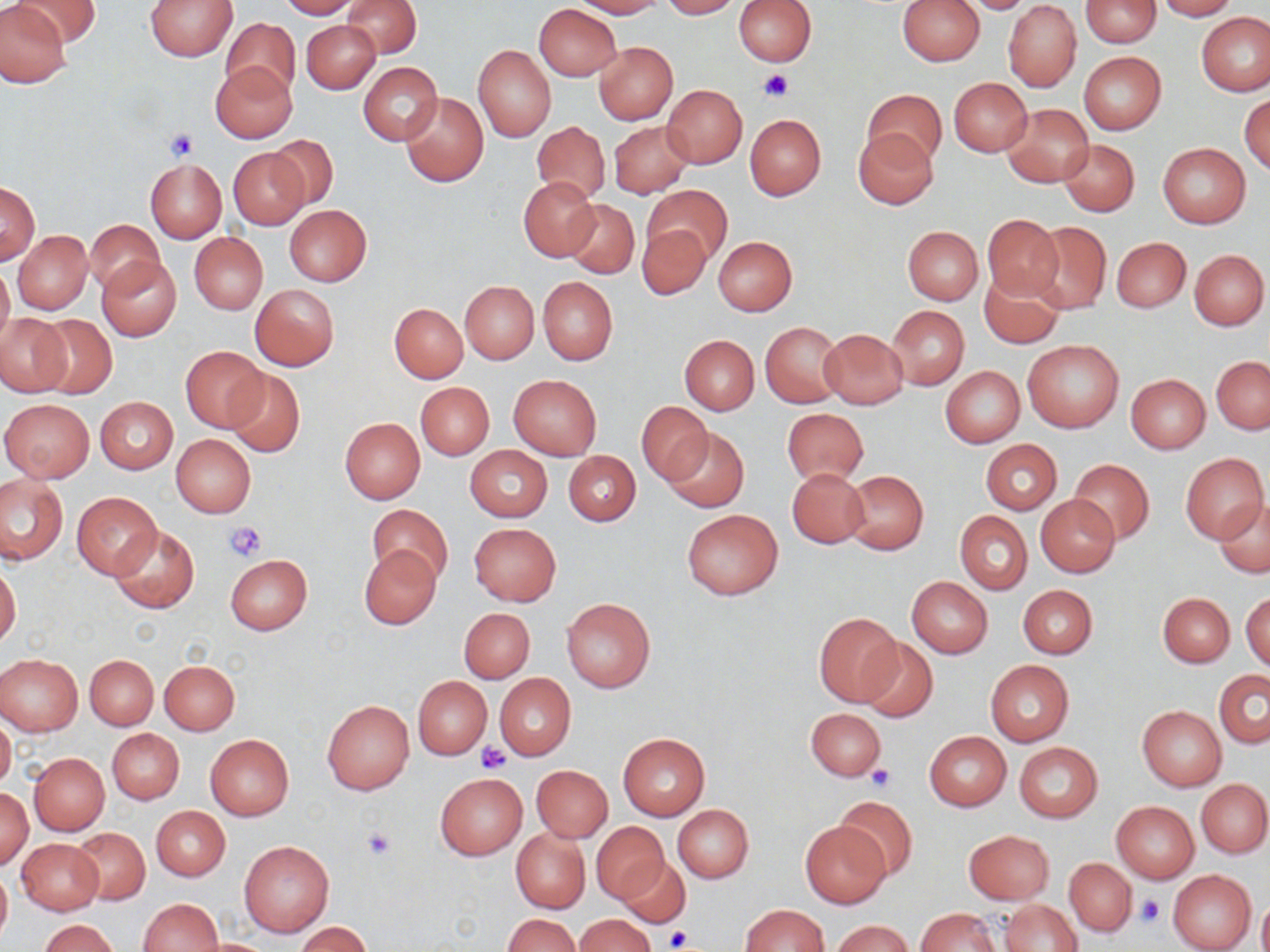

slide-level diagnosis = no evidence of blood parasites
image size = 1270×952 pixels
platelet locations = approximate bounding boxes as (x1, y1, x2, y2) in pixels: (757, 68, 794, 102), (164, 129, 200, 161), (226, 521, 266, 562), (477, 743, 510, 772), (866, 764, 894, 792), (358, 826, 398, 862), (1137, 894, 1165, 927), (666, 927, 691, 950)
magnification = 1000x
modality = optical microscopy
field of view = one of a larger specimen
preparation = thin blood smear
stain = May-Grünwald-Giemsa
uninfected red blood cell locations = approximate bounding boxes as (x1, y1, x2, y2) in pixels: (11, 0, 102, 46), (144, 0, 237, 60), (279, 0, 358, 18), (571, 0, 664, 18), (659, 0, 744, 19), (897, 0, 985, 65), (959, 0, 1037, 14), (1003, 0, 1082, 92), (1081, 0, 1161, 48), (1154, 0, 1239, 20), (0, 1, 72, 87), (343, 1, 421, 59), (734, 1, 815, 64), (534, 4, 621, 81), (1196, 12, 1269, 95), (220, 18, 300, 101), (301, 20, 380, 93), (593, 42, 677, 124), (473, 44, 556, 142), (1079, 52, 1165, 134), (210, 61, 297, 143), (358, 61, 442, 146), (949, 78, 1031, 156), (663, 86, 746, 167), (864, 88, 946, 167), (401, 92, 488, 187), (1240, 93, 1269, 174), (1002, 103, 1093, 187), (745, 113, 826, 200), (533, 120, 610, 206), (609, 121, 693, 197), (853, 129, 939, 210), (269, 136, 339, 210), (1058, 138, 1140, 217), (1157, 143, 1250, 228), (228, 147, 309, 229), (146, 159, 227, 242), (519, 178, 600, 261), (1, 182, 39, 264), (644, 185, 731, 263), (563, 200, 640, 279), (284, 205, 372, 286), (980, 213, 1061, 300), (85, 219, 165, 294), (1028, 221, 1111, 314), (637, 223, 710, 300), (902, 226, 983, 305), (13, 231, 91, 314), (190, 232, 267, 314), (713, 236, 797, 315), (1111, 237, 1190, 313), (1189, 248, 1268, 330), (97, 257, 182, 342), (0, 262, 14, 348), (980, 272, 1065, 348), (538, 277, 617, 365), (460, 280, 539, 363), (250, 284, 339, 371), (390, 303, 468, 382), (887, 306, 968, 389), (33, 312, 117, 399), (1, 313, 71, 395), (761, 322, 845, 408), (819, 328, 909, 409), (679, 335, 759, 414), (1023, 340, 1123, 433), (179, 345, 269, 433), (1211, 356, 1270, 434), (939, 365, 1025, 449), (224, 368, 305, 457), (509, 374, 601, 459), (1126, 374, 1210, 453), (416, 382, 495, 460), (96, 396, 177, 473), (1, 399, 94, 482), (636, 401, 710, 485), (782, 408, 869, 485), (340, 417, 425, 503), (660, 427, 749, 513), (170, 434, 255, 518), (980, 439, 1062, 514), (466, 446, 552, 522), (1180, 452, 1268, 543), (564, 453, 641, 526), (1068, 459, 1155, 545), (787, 468, 869, 547), (842, 469, 929, 554), (0, 476, 67, 563), (72, 494, 162, 579), (1035, 494, 1120, 579), (1215, 499, 1270, 577), (367, 503, 453, 585), (683, 509, 782, 599), (955, 511, 1032, 595), (469, 522, 561, 606), (110, 525, 200, 615), (359, 545, 442, 630), (225, 554, 312, 635), (0, 562, 21, 647), (907, 576, 993, 658), (1018, 584, 1097, 660), (1242, 592, 1270, 673), (1158, 593, 1234, 667), (561, 596, 656, 693), (459, 608, 535, 682), (814, 612, 903, 706), (857, 637, 938, 723), (0, 653, 82, 735), (85, 654, 158, 729), (160, 660, 240, 735), (986, 660, 1074, 745), (1214, 669, 1270, 749), (495, 674, 575, 760), (413, 675, 491, 760), (322, 699, 414, 794), (1137, 706, 1226, 791), (806, 707, 886, 781), (0, 715, 16, 792), (108, 728, 184, 803), (924, 730, 1011, 810), (618, 733, 709, 819), (205, 734, 294, 820), (1014, 742, 1103, 822), (29, 753, 109, 834), (531, 765, 612, 842), (434, 771, 525, 860), (1197, 780, 1270, 856), (0, 789, 33, 869), (833, 795, 916, 879), (1111, 801, 1199, 883), (673, 804, 754, 883), (152, 806, 230, 881), (799, 821, 890, 908), (592, 822, 669, 903), (71, 827, 149, 904), (511, 828, 590, 914), (963, 829, 1055, 905), (17, 839, 103, 914), (240, 840, 334, 935), (619, 856, 690, 927), (1064, 858, 1137, 937), (0, 863, 11, 947), (1167, 869, 1257, 952), (1258, 896, 1270, 952), (138, 898, 223, 952), (999, 900, 1083, 952), (740, 904, 829, 951), (915, 907, 1000, 952), (503, 914, 580, 951), (575, 914, 653, 952), (38, 919, 118, 952), (833, 920, 912, 952), (296, 922, 370, 952)